Assess for malaria.
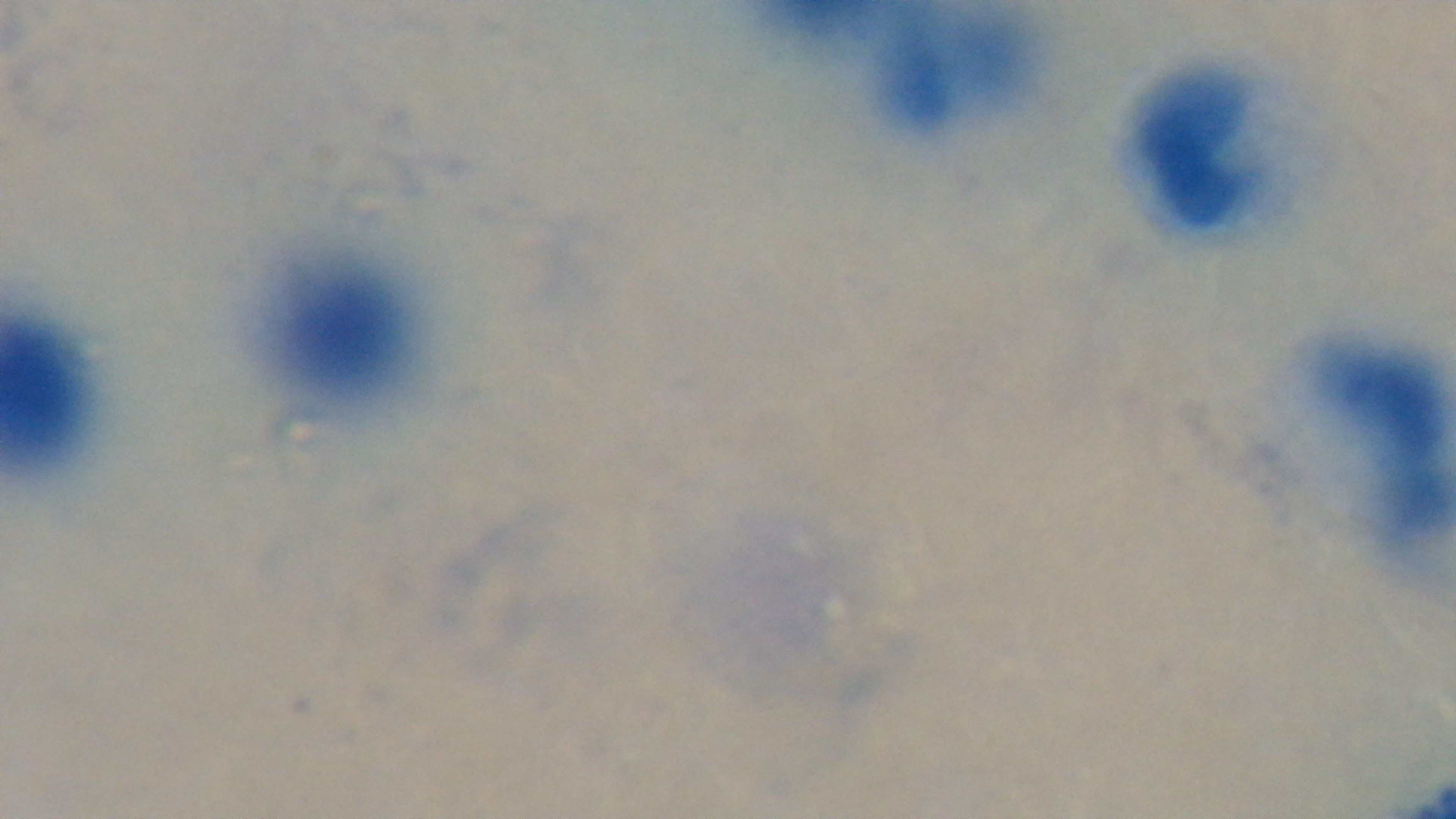
It is uninfected.

stain = Giemsa
objective = 100x oil immersion
modality = light microscopy
capture = mounted 4K digital camera
preparation = thick smear
field of view = single